Give the position of each Plasmodium falciparum parasite with its life-cycle stage, each leukocyte, and any debris.
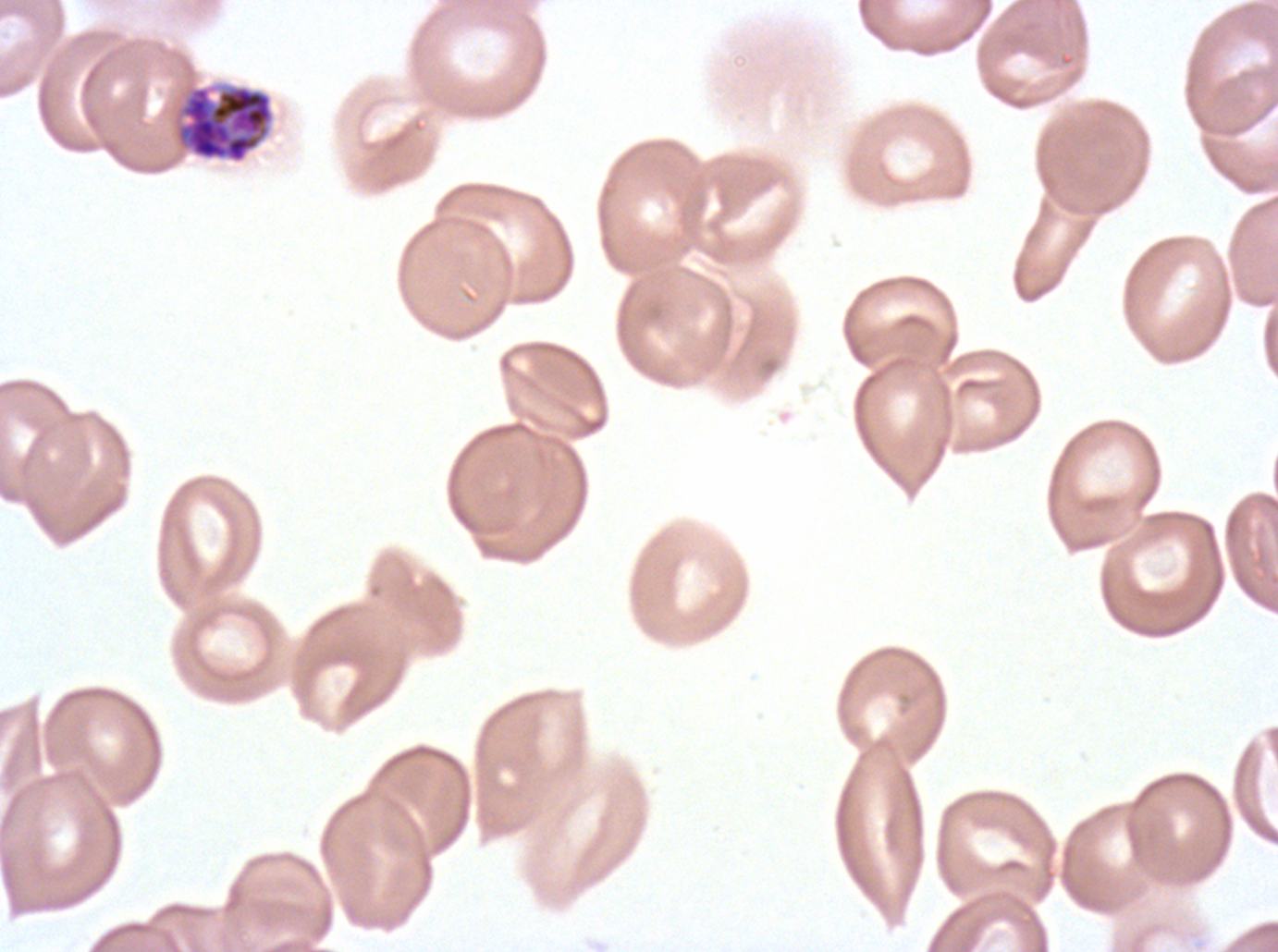

Approximate bounding boxes as [x1, y1, x2, y2] in pixels.
Segmenters: [173, 83, 276, 165].
No rings, late-ring/early-trophozoite forms, mid trophozoites, late trophozoites, early schizonts, late schizonts, gametocytes, leukocytes, or debris observed.

field of view = one sub-image of a larger composite
preparation = thin blood smear
image size = 1278×952 pixels
stain = Giemsa
specimen = ex-vivo Plasmodium falciparum culture from a patient in The Gambia, grown for 24 to 48 hours